Identify the parasite.
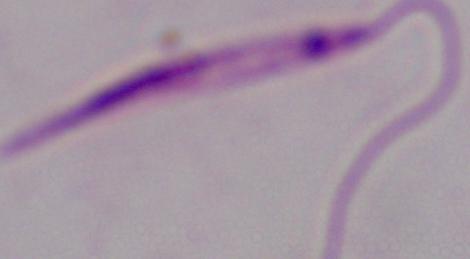
Leishmania.

modality: photomicrograph
magnification: 1000x